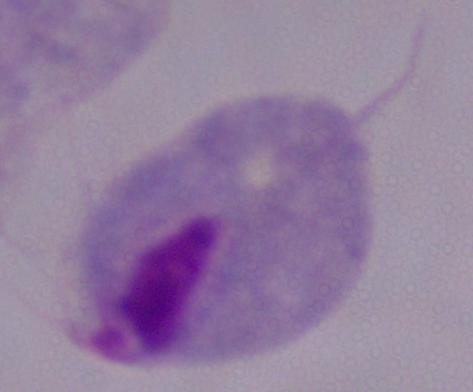

Photomicrograph. 1000x magnification. A trichomonad is shown.